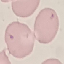
Malaria status: uninfected. Cell patch, automatically extracted from a larger field of view and resized to 64 × 64 pixels. Photographed with a smartphone camera at the microscope eyepiece. Giemsa-stained preparation. Thin blood film.